Locate every blood parasite and identify its species.
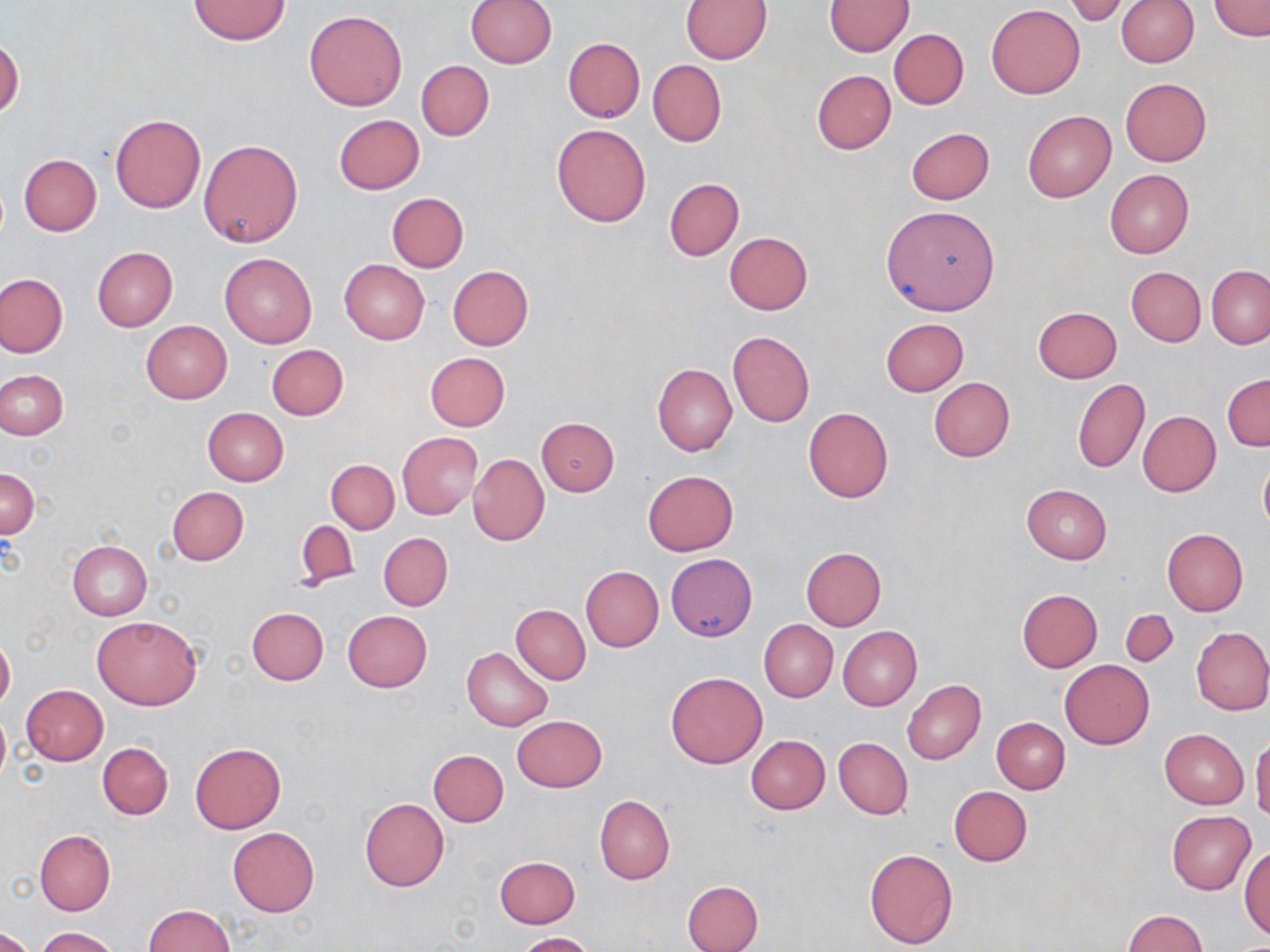

No blood parasites seen.

Approximate bounding boxes as (x1, y1, x2, y2) in pixels. Uninfected red blood cell locations: (681, 0, 771, 63), (1116, 0, 1198, 67), (189, 1, 288, 45), (466, 1, 556, 69), (825, 1, 914, 56), (1062, 1, 1136, 26), (1208, 1, 1270, 39), (986, 4, 1084, 98), (304, 10, 408, 110), (889, 28, 969, 109), (1, 37, 23, 119), (563, 37, 644, 122), (416, 59, 494, 141), (647, 59, 726, 146), (813, 70, 895, 154), (1119, 78, 1212, 166), (1023, 110, 1116, 201), (110, 112, 206, 213), (333, 115, 425, 195), (551, 124, 651, 227), (906, 127, 995, 205), (198, 138, 303, 249), (18, 154, 101, 236), (1105, 170, 1192, 257), (665, 178, 743, 260), (386, 193, 468, 273), (881, 205, 1000, 316), (725, 232, 812, 314), (92, 247, 177, 331), (219, 252, 317, 348), (339, 259, 429, 344), (447, 265, 533, 351), (1126, 266, 1206, 346), (1207, 266, 1270, 349), (0, 273, 67, 357), (1032, 306, 1122, 383), (880, 318, 968, 396), (142, 321, 231, 403), (728, 332, 814, 426), (266, 344, 348, 419), (425, 352, 510, 431), (652, 364, 736, 456), (0, 369, 68, 440), (1222, 373, 1270, 450), (928, 377, 1015, 461), (1073, 379, 1149, 474), (803, 407, 893, 503), (202, 408, 288, 487), (1137, 410, 1221, 496), (536, 417, 619, 496), (397, 432, 482, 519), (468, 453, 549, 546), (1258, 453, 1270, 535), (326, 459, 399, 534), (1, 468, 39, 537), (642, 470, 739, 555), (1021, 484, 1112, 564), (167, 486, 249, 566), (294, 521, 359, 591), (1162, 528, 1248, 617), (379, 533, 452, 610), (67, 541, 151, 621), (801, 547, 886, 630), (666, 554, 756, 641), (580, 565, 664, 651), (1017, 589, 1101, 672), (511, 604, 590, 684), (247, 607, 328, 684), (1121, 610, 1177, 665), (342, 611, 431, 692), (92, 615, 202, 709), (758, 620, 837, 702), (837, 626, 921, 712), (1191, 626, 1270, 715), (0, 635, 14, 712), (462, 647, 553, 731), (1060, 660, 1154, 749), (666, 671, 767, 769), (902, 680, 986, 764), (21, 685, 109, 765), (0, 705, 11, 789), (511, 716, 607, 793), (991, 717, 1069, 793), (1159, 728, 1248, 808), (746, 735, 830, 814), (1251, 735, 1270, 822), (834, 736, 913, 820), (98, 742, 173, 819), (189, 743, 286, 834), (428, 750, 509, 826), (949, 786, 1032, 866), (594, 795, 674, 884), (359, 798, 449, 891), (1167, 811, 1255, 894), (228, 827, 319, 916), (34, 829, 115, 915), (1239, 846, 1269, 939), (864, 848, 959, 950), (495, 857, 579, 929), (682, 879, 764, 952), (142, 904, 235, 952), (1124, 910, 1209, 952), (0, 927, 35, 952), (34, 927, 120, 952), (516, 931, 599, 952). Slide-level diagnosis: no evidence of blood parasites. May-Grünwald-Giemsa stain. Image is 1270×952 pixels. 1000x magnification. Single field of view. Thin blood smear. Light microscopy.